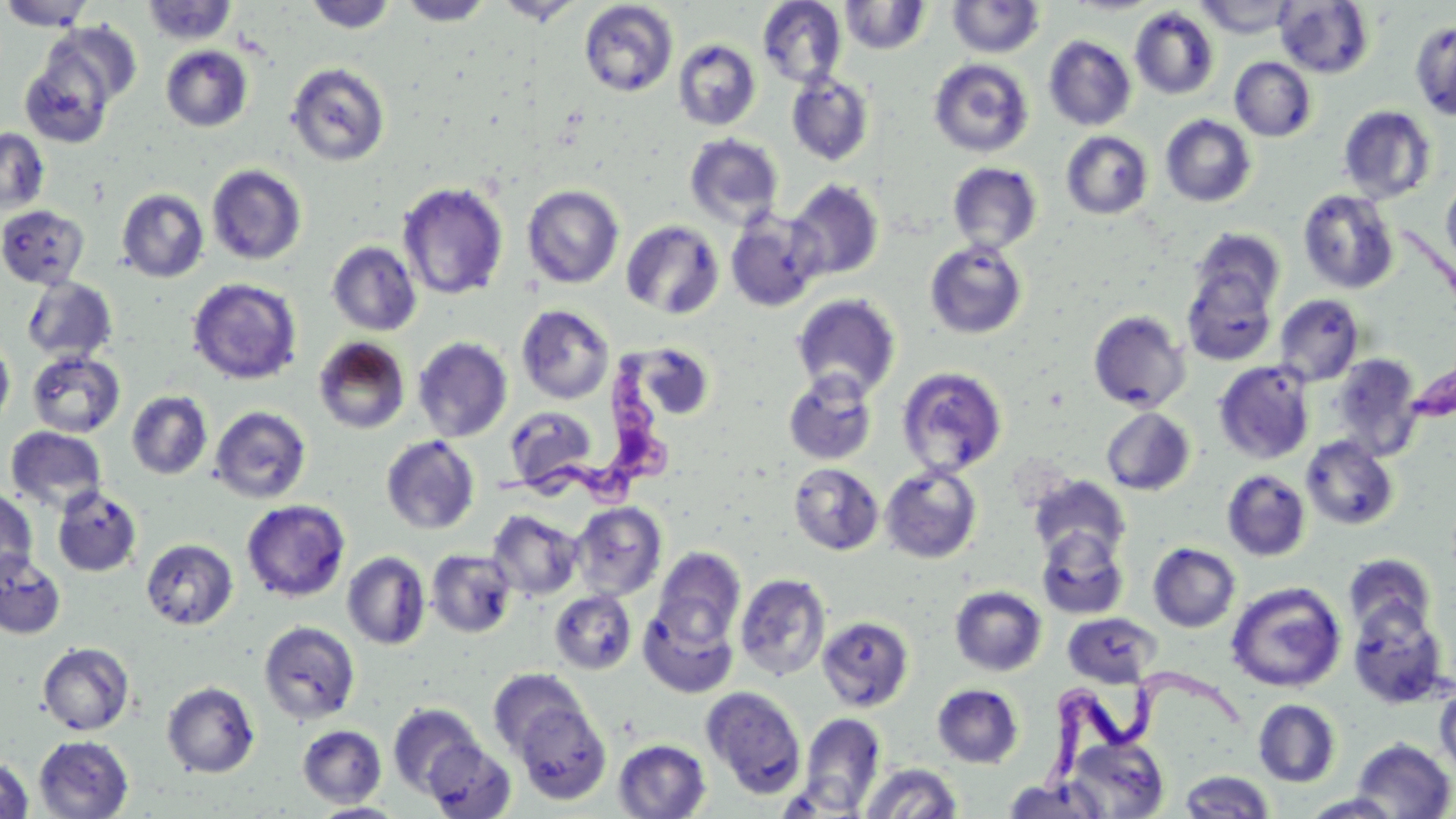

slide-level diagnosis = Trypanosoma brucei
magnification = 1000x
modality = optical microscopy
uninfected red blood cell locations = approximate bounding boxes as named x1/y1/x2/y2 corners in pixels: (x1=0, y1=0, x2=97, y2=30), (x1=396, y1=0, x2=495, y2=26), (x1=495, y1=0, x2=585, y2=25), (x1=1195, y1=0, x2=1298, y2=38), (x1=141, y1=1, x2=238, y2=45), (x1=304, y1=1, x2=398, y2=33), (x1=578, y1=1, x2=678, y2=97), (x1=757, y1=1, x2=846, y2=87), (x1=838, y1=1, x2=931, y2=55), (x1=947, y1=1, x2=1045, y2=58), (x1=1275, y1=1, x2=1374, y2=78), (x1=1130, y1=6, x2=1219, y2=100), (x1=1411, y1=20, x2=1456, y2=120), (x1=1044, y1=35, x2=1136, y2=131), (x1=673, y1=38, x2=761, y2=131), (x1=19, y1=44, x2=119, y2=149), (x1=161, y1=45, x2=253, y2=132), (x1=1230, y1=57, x2=1316, y2=141), (x1=928, y1=58, x2=1034, y2=157), (x1=286, y1=62, x2=390, y2=167), (x1=787, y1=72, x2=875, y2=166), (x1=1338, y1=105, x2=1437, y2=204), (x1=1160, y1=115, x2=1256, y2=207), (x1=0, y1=128, x2=50, y2=214), (x1=1061, y1=131, x2=1153, y2=220), (x1=684, y1=133, x2=784, y2=229), (x1=947, y1=162, x2=1042, y2=254), (x1=207, y1=164, x2=307, y2=264), (x1=1441, y1=172, x2=1456, y2=275), (x1=787, y1=179, x2=884, y2=280), (x1=397, y1=182, x2=509, y2=300), (x1=522, y1=185, x2=624, y2=288), (x1=117, y1=188, x2=209, y2=282), (x1=1298, y1=189, x2=1400, y2=294), (x1=0, y1=205, x2=90, y2=289), (x1=725, y1=209, x2=826, y2=312), (x1=621, y1=220, x2=724, y2=319), (x1=1190, y1=228, x2=1286, y2=313), (x1=924, y1=240, x2=1028, y2=339), (x1=326, y1=241, x2=422, y2=336), (x1=1182, y1=267, x2=1278, y2=365), (x1=22, y1=276, x2=118, y2=363), (x1=188, y1=278, x2=302, y2=385), (x1=791, y1=294, x2=901, y2=399), (x1=1274, y1=295, x2=1364, y2=386), (x1=516, y1=304, x2=615, y2=404), (x1=1089, y1=310, x2=1190, y2=412), (x1=0, y1=335, x2=15, y2=428), (x1=313, y1=336, x2=411, y2=435), (x1=413, y1=337, x2=513, y2=442), (x1=632, y1=341, x2=716, y2=420), (x1=27, y1=350, x2=125, y2=438), (x1=1330, y1=354, x2=1423, y2=461), (x1=1213, y1=362, x2=1314, y2=464), (x1=896, y1=366, x2=1008, y2=477), (x1=783, y1=371, x2=878, y2=466), (x1=127, y1=391, x2=213, y2=479), (x1=504, y1=405, x2=599, y2=491), (x1=209, y1=406, x2=312, y2=504), (x1=1101, y1=407, x2=1195, y2=495), (x1=5, y1=426, x2=107, y2=514), (x1=381, y1=435, x2=480, y2=535), (x1=1301, y1=436, x2=1399, y2=531), (x1=788, y1=463, x2=884, y2=555), (x1=880, y1=464, x2=982, y2=563), (x1=1222, y1=469, x2=1311, y2=561), (x1=1028, y1=475, x2=1131, y2=562), (x1=52, y1=486, x2=143, y2=577), (x1=0, y1=487, x2=37, y2=581), (x1=241, y1=499, x2=350, y2=602), (x1=570, y1=502, x2=667, y2=601), (x1=487, y1=510, x2=583, y2=600), (x1=1036, y1=527, x2=1129, y2=619), (x1=141, y1=538, x2=238, y2=630), (x1=1148, y1=543, x2=1240, y2=632), (x1=653, y1=548, x2=746, y2=648), (x1=426, y1=549, x2=517, y2=637), (x1=0, y1=550, x2=66, y2=640), (x1=342, y1=551, x2=431, y2=650), (x1=1343, y1=553, x2=1437, y2=639), (x1=734, y1=573, x2=831, y2=681), (x1=1226, y1=582, x2=1346, y2=692), (x1=950, y1=586, x2=1047, y2=676), (x1=550, y1=589, x2=637, y2=674), (x1=548, y1=594, x2=738, y2=678), (x1=1347, y1=600, x2=1451, y2=709), (x1=639, y1=601, x2=739, y2=698), (x1=1062, y1=612, x2=1162, y2=688), (x1=817, y1=616, x2=914, y2=712), (x1=258, y1=620, x2=361, y2=725), (x1=37, y1=642, x2=135, y2=735), (x1=488, y1=668, x2=588, y2=758), (x1=162, y1=681, x2=260, y2=778), (x1=1435, y1=683, x2=1456, y2=781), (x1=932, y1=684, x2=1024, y2=768), (x1=701, y1=686, x2=807, y2=799), (x1=1253, y1=699, x2=1341, y2=788), (x1=513, y1=701, x2=613, y2=805), (x1=388, y1=703, x2=484, y2=796), (x1=799, y1=712, x2=886, y2=813), (x1=297, y1=725, x2=386, y2=807), (x1=34, y1=735, x2=133, y2=818), (x1=1066, y1=736, x2=1169, y2=817), (x1=1351, y1=738, x2=1455, y2=818), (x1=613, y1=739, x2=711, y2=818), (x1=423, y1=740, x2=516, y2=819), (x1=0, y1=755, x2=34, y2=819), (x1=860, y1=763, x2=963, y2=817), (x1=1178, y1=770, x2=1277, y2=818), (x1=1001, y1=778, x2=1110, y2=818), (x1=1301, y1=793, x2=1407, y2=818), (x1=311, y1=802, x2=406, y2=818)
image size = 1456×819 pixels
Trypanosoma brucei locations = approximate bounding boxes as named x1/y1/x2/y2 corners in pixels: (x1=492, y1=345, x2=677, y2=510), (x1=1031, y1=671, x2=1248, y2=801)
preparation = thin blood smear
field of view = single
stain = May-Grünwald-Giemsa